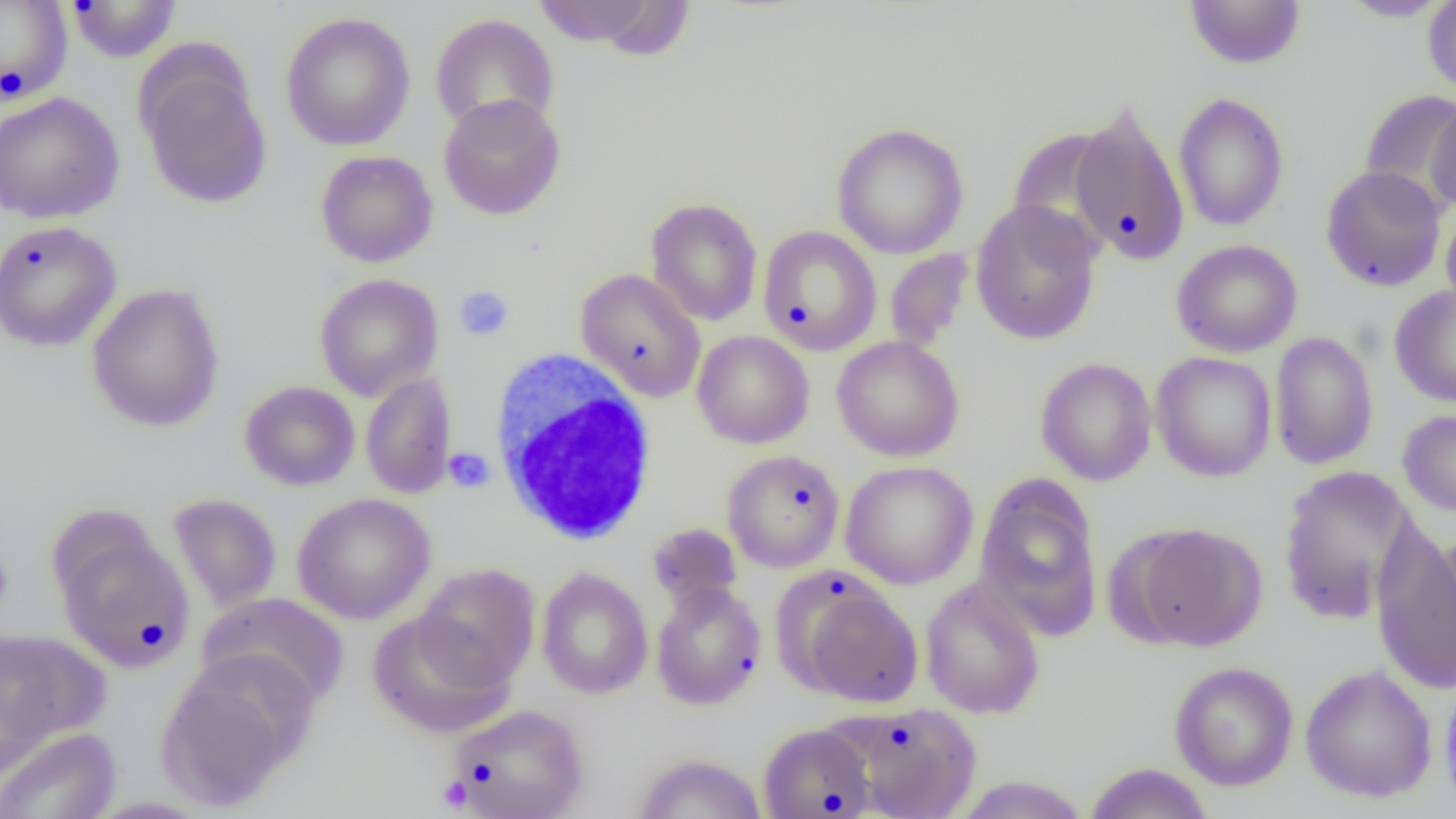

slide-level diagnosis = no evidence of blood parasites
magnification = 1000x
uninfected red blood cell locations = approximate bounding boxes as (x1, y1, x2, y2) in pixels: (67, 0, 180, 63), (530, 0, 671, 51), (1184, 0, 1306, 70), (1422, 0, 1456, 96), (0, 1, 72, 105), (1335, 1, 1453, 22), (280, 12, 416, 151), (430, 13, 559, 135), (137, 58, 273, 209), (1357, 88, 1456, 213), (0, 92, 125, 224), (1172, 92, 1290, 232), (438, 93, 566, 221), (1426, 96, 1456, 217), (1066, 102, 1191, 266), (831, 122, 969, 259), (1007, 122, 1125, 256), (315, 150, 438, 268), (1320, 165, 1447, 292), (645, 197, 763, 326), (970, 199, 1103, 345), (1440, 206, 1456, 318), (0, 220, 123, 352), (758, 226, 882, 355), (1171, 239, 1303, 358), (884, 250, 974, 353), (575, 268, 707, 403), (314, 273, 444, 401), (87, 283, 225, 433), (1389, 284, 1456, 407), (692, 330, 815, 449), (1268, 331, 1379, 470), (831, 335, 964, 462), (1151, 351, 1277, 482), (1034, 357, 1157, 486), (361, 372, 457, 499), (239, 381, 360, 491), (1398, 409, 1456, 517), (722, 449, 845, 573), (839, 461, 978, 589), (1277, 465, 1421, 624), (975, 478, 1103, 641), (168, 493, 282, 611), (292, 493, 435, 624), (647, 522, 743, 610), (1127, 522, 1268, 652), (1370, 525, 1456, 695), (55, 531, 195, 672), (413, 562, 540, 689), (536, 568, 653, 700), (920, 577, 1046, 719), (792, 578, 923, 708), (651, 582, 767, 711), (197, 592, 349, 710), (366, 611, 515, 739), (0, 629, 108, 752), (156, 654, 313, 811), (1169, 661, 1299, 791), (1299, 664, 1438, 803), (1439, 676, 1456, 814), (448, 703, 590, 819), (850, 703, 981, 818), (758, 723, 875, 818), (0, 727, 120, 819), (632, 752, 767, 818), (1083, 763, 1214, 819), (950, 775, 1091, 818), (85, 797, 212, 818)
platelet locations = approximate bounding boxes as (x1, y1, x2, y2) in pixels: (454, 286, 514, 341), (444, 447, 495, 493), (437, 776, 473, 812)
white blood cell locations = approximate bounding boxes as (x1, y1, x2, y2) in pixels: (489, 351, 660, 546)
modality = light microscopy
image size = 1456×819 pixels
field of view = one of a larger specimen
preparation = thin blood film